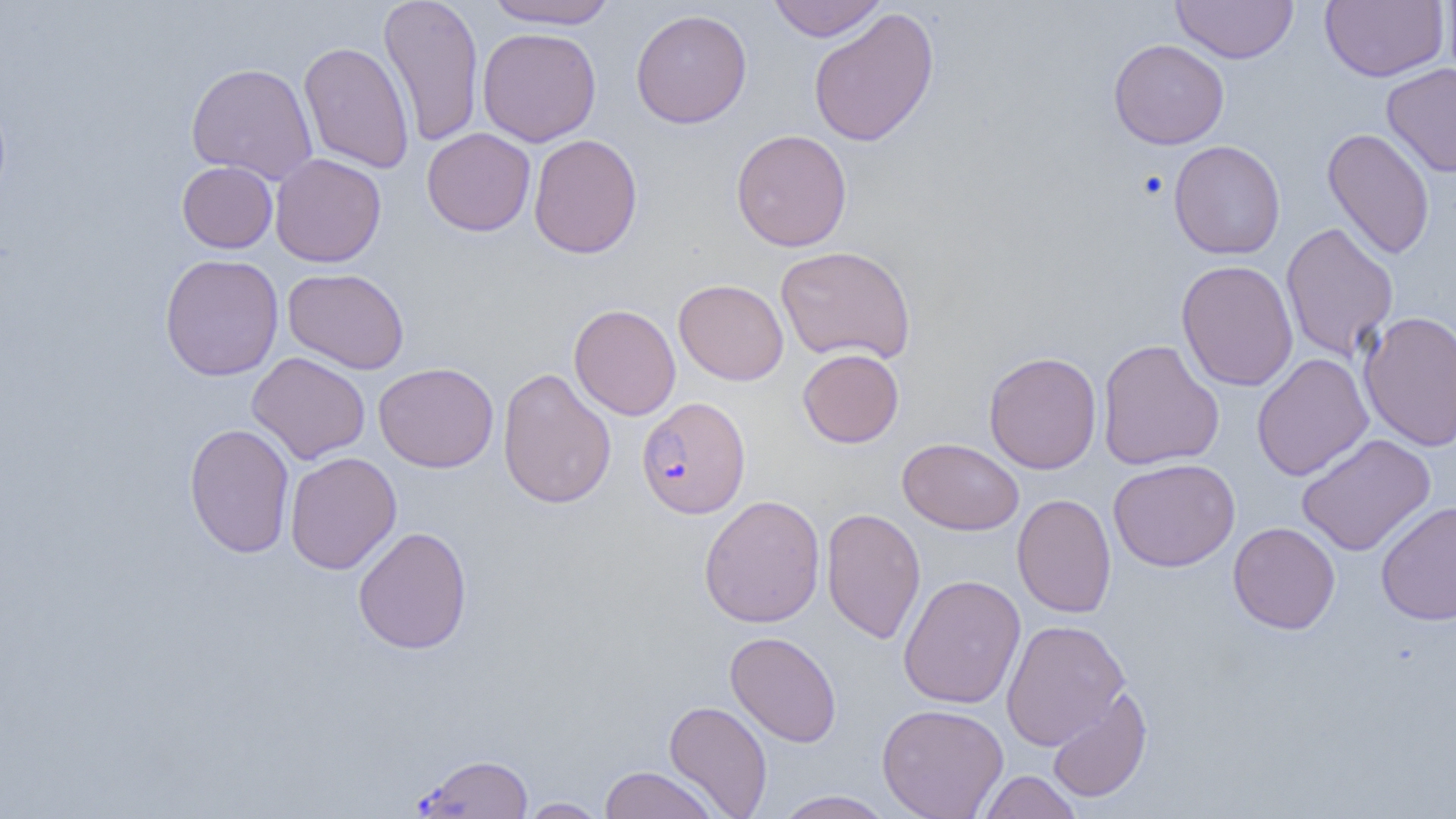

slide-level diagnosis = Plasmodium falciparum
image size = 1456×819 pixels
modality = light microscopy
uninfected red blood cell locations = approximate bounding boxes as (x1,y1)-(x2,y2) corner pairs in pixels: (378,0)-(484,147), (483,0)-(617,29), (767,0)-(887,42), (1320,0)-(1448,82), (1442,0)-(1456,84), (1171,1)-(1298,63), (630,8)-(752,129), (808,8)-(939,148), (477,27)-(602,147), (1108,38)-(1229,150), (298,41)-(414,173), (186,62)-(318,184), (1381,62)-(1456,178), (422,127)-(536,236), (1321,127)-(1435,260), (731,129)-(852,252), (528,133)-(643,259), (1169,140)-(1286,260), (269,153)-(387,267), (177,160)-(278,253), (1280,222)-(1399,362), (775,245)-(917,365), (159,254)-(284,381), (1176,260)-(1298,391), (282,267)-(409,374), (674,279)-(789,385), (568,304)-(681,420), (1358,310)-(1456,452), (1097,338)-(1225,471), (797,348)-(904,448), (984,351)-(1102,474), (247,352)-(370,464), (1251,353)-(1373,481), (374,361)-(499,473), (497,368)-(616,510), (184,423)-(295,559), (1295,433)-(1436,556), (897,438)-(1024,536), (285,451)-(402,574), (1108,458)-(1240,572), (1012,493)-(1117,618), (699,494)-(826,628), (1376,500)-(1456,626), (821,507)-(926,644), (1227,521)-(1341,634), (352,526)-(473,655), (898,574)-(1026,709), (1001,619)-(1130,750), (725,631)-(842,748), (1046,687)-(1152,803), (663,700)-(773,817), (877,703)-(1009,819), (598,765)-(721,819), (978,771)-(1083,819), (772,790)-(897,819), (517,797)-(610,818)
Plasmodium falciparum-infected red blood cell locations = approximate bounding boxes as (x1,y1)-(x2,y2) corner pairs in pixels: (636,397)-(751,519), (414,753)-(533,818)
field of view = one of a larger specimen
preparation = thin blood smear
platelet locations = approximate bounding boxes as (x1,y1)-(x2,y2) corner pairs in pixels: (1137,171)-(1169,200)
magnification = 1000x